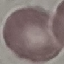
malaria_status: uninfected
stain: Giemsa
capture: smartphone camera at the microscope eyepiece
image_type: cell patch, automatically extracted from a larger field of view and resized to 64 × 64 pixels
preparation: thin blood smear